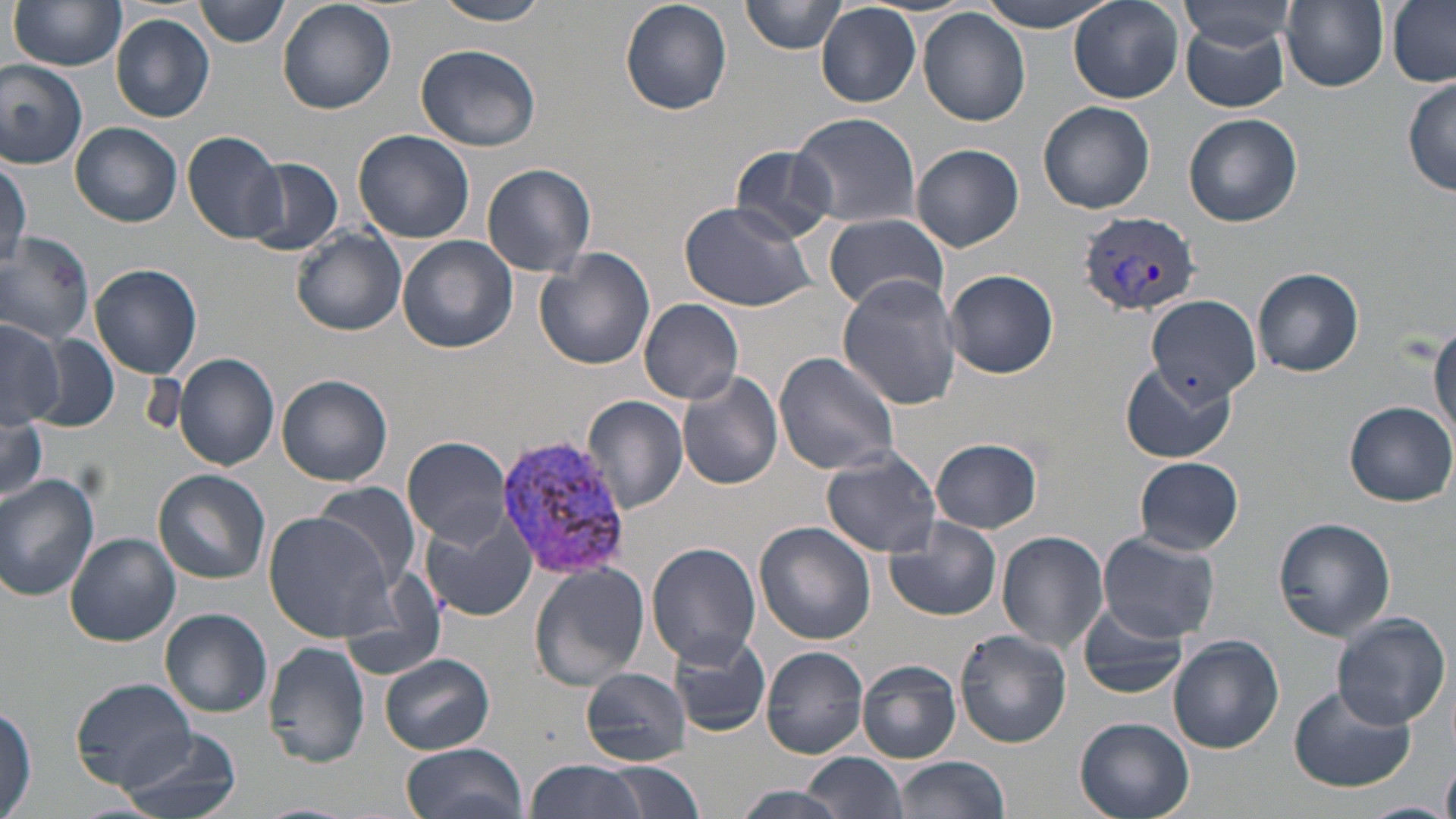

{
  "slide_level_diagnosis": "Plasmodium vivax",
  "uninfected_red_blood_cell_locations": "approximate bounding boxes as named x1/y1/x2/y2 corners in pixels: (x1=195, y1=0, x2=290, y2=46), (x1=277, y1=0, x2=395, y2=113), (x1=433, y1=0, x2=555, y2=26), (x1=620, y1=0, x2=732, y2=116), (x1=741, y1=0, x2=845, y2=54), (x1=979, y1=0, x2=1113, y2=30), (x1=9, y1=1, x2=127, y2=71), (x1=1069, y1=1, x2=1184, y2=105), (x1=1177, y1=1, x2=1297, y2=59), (x1=1280, y1=1, x2=1390, y2=91), (x1=1388, y1=2, x2=1455, y2=86), (x1=817, y1=4, x2=920, y2=107), (x1=918, y1=8, x2=1031, y2=128), (x1=111, y1=14, x2=215, y2=122), (x1=1179, y1=17, x2=1291, y2=112), (x1=416, y1=42, x2=544, y2=152), (x1=0, y1=60, x2=88, y2=168), (x1=1401, y1=77, x2=1455, y2=197), (x1=1037, y1=100, x2=1156, y2=214), (x1=792, y1=111, x2=920, y2=228), (x1=1183, y1=113, x2=1302, y2=227), (x1=72, y1=122, x2=182, y2=227), (x1=182, y1=130, x2=286, y2=244), (x1=353, y1=130, x2=474, y2=244), (x1=912, y1=143, x2=1023, y2=252), (x1=727, y1=144, x2=841, y2=241), (x1=244, y1=157, x2=342, y2=255), (x1=0, y1=161, x2=29, y2=269), (x1=482, y1=162, x2=597, y2=277), (x1=679, y1=199, x2=818, y2=311), (x1=823, y1=213, x2=949, y2=312), (x1=293, y1=228, x2=405, y2=336), (x1=0, y1=230, x2=96, y2=344), (x1=398, y1=236, x2=519, y2=354), (x1=535, y1=248, x2=656, y2=371), (x1=90, y1=264, x2=202, y2=379), (x1=1254, y1=267, x2=1363, y2=378), (x1=944, y1=268, x2=1060, y2=379), (x1=837, y1=275, x2=963, y2=411), (x1=1145, y1=296, x2=1262, y2=403), (x1=639, y1=297, x2=745, y2=403), (x1=0, y1=320, x2=63, y2=430), (x1=1430, y1=322, x2=1456, y2=442), (x1=25, y1=333, x2=120, y2=434), (x1=772, y1=349, x2=901, y2=475), (x1=173, y1=353, x2=280, y2=472), (x1=1120, y1=360, x2=1236, y2=464), (x1=678, y1=372, x2=785, y2=490), (x1=277, y1=375, x2=393, y2=486), (x1=788, y1=389, x2=910, y2=534), (x1=581, y1=395, x2=688, y2=515), (x1=1342, y1=400, x2=1455, y2=507), (x1=0, y1=409, x2=46, y2=504), (x1=403, y1=436, x2=514, y2=546), (x1=931, y1=439, x2=1042, y2=533), (x1=821, y1=448, x2=946, y2=561), (x1=1134, y1=456, x2=1243, y2=556), (x1=154, y1=469, x2=271, y2=584), (x1=0, y1=474, x2=102, y2=601), (x1=312, y1=480, x2=422, y2=590), (x1=265, y1=512, x2=401, y2=644), (x1=421, y1=514, x2=539, y2=623), (x1=884, y1=516, x2=1002, y2=621), (x1=1272, y1=516, x2=1397, y2=643), (x1=753, y1=522, x2=875, y2=646), (x1=998, y1=531, x2=1109, y2=652), (x1=1098, y1=532, x2=1220, y2=643), (x1=66, y1=534, x2=180, y2=646), (x1=646, y1=543, x2=762, y2=666), (x1=527, y1=563, x2=650, y2=691), (x1=1075, y1=600, x2=1188, y2=700), (x1=159, y1=608, x2=273, y2=718), (x1=1331, y1=612, x2=1451, y2=730), (x1=954, y1=629, x2=1071, y2=748), (x1=669, y1=632, x2=770, y2=738), (x1=1168, y1=635, x2=1285, y2=754), (x1=263, y1=641, x2=370, y2=767), (x1=763, y1=647, x2=868, y2=757), (x1=378, y1=653, x2=495, y2=754), (x1=857, y1=658, x2=963, y2=763), (x1=581, y1=668, x2=691, y2=764), (x1=72, y1=678, x2=196, y2=788), (x1=1286, y1=684, x2=1417, y2=794), (x1=0, y1=705, x2=36, y2=819), (x1=1075, y1=716, x2=1195, y2=819), (x1=118, y1=726, x2=241, y2=819), (x1=402, y1=743, x2=529, y2=819), (x1=802, y1=752, x2=908, y2=819), (x1=891, y1=756, x2=1009, y2=819), (x1=524, y1=758, x2=650, y2=819), (x1=1442, y1=758, x2=1456, y2=819), (x1=600, y1=762, x2=708, y2=819), (x1=726, y1=784, x2=854, y2=819), (x1=1353, y1=801, x2=1456, y2=819)",
  "preparation": "thin blood smear",
  "plasmodium_vivax_infected_red_blood_cell_locations": "approximate bounding boxes as named x1/y1/x2/y2 corners in pixels: (x1=1077, y1=211, x2=1202, y2=316), (x1=499, y1=431, x2=631, y2=579)",
  "stain": "May-Grünwald-Giemsa",
  "magnification": "1000x",
  "image_size": "1456×819 pixels",
  "field_of_view": "single",
  "modality": "light microscopy"
}